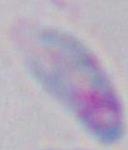
Summary:
  - Modality: micrograph
  - Identification: Toxoplasma gondii
  - Magnification: 1000x